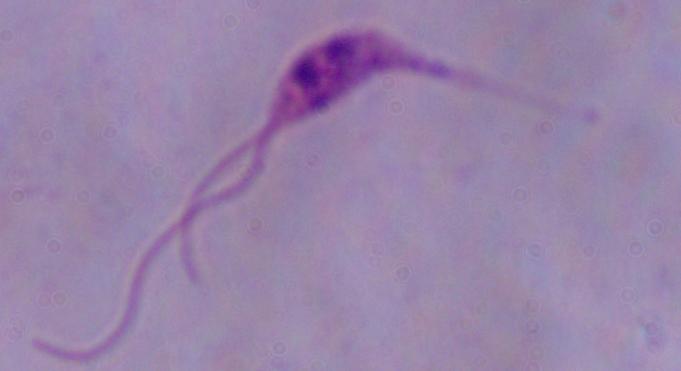

magnification = 1000x
modality = micrograph
identification = Leishmania